Locate every malaria parasite.
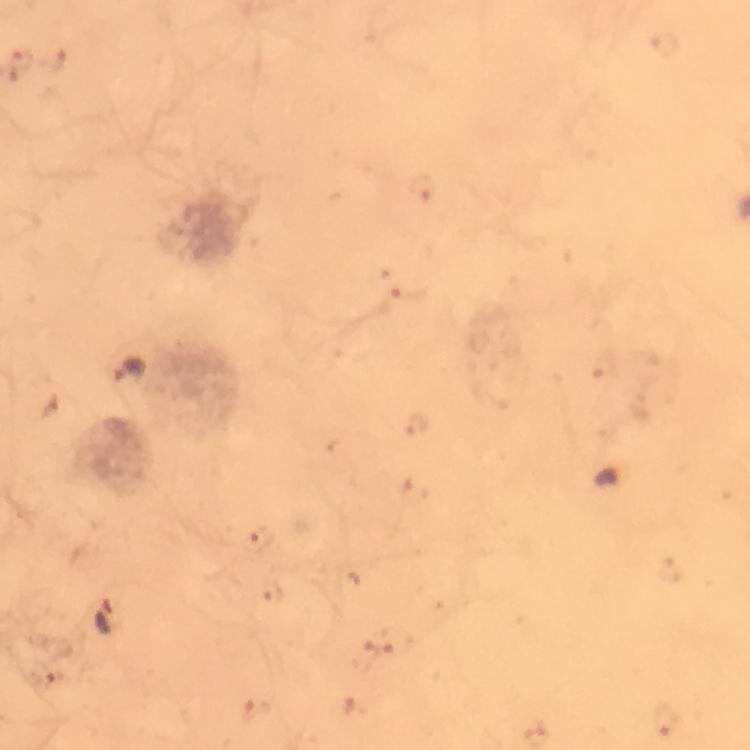

Approximate object centers, in pixels from the top-left corner.
Malaria parasites: (x=130, y=371), (x=106, y=619).

From a diagnostic examination for malaria. Photographed with a smartphone mounted on the microscope. Image is 750×750 pixels. At 100x magnification. Thick smear. A crop from one field of view. Immersion oil applied. Giemsa stain.